Comment on the morphology of the erythrocytes.
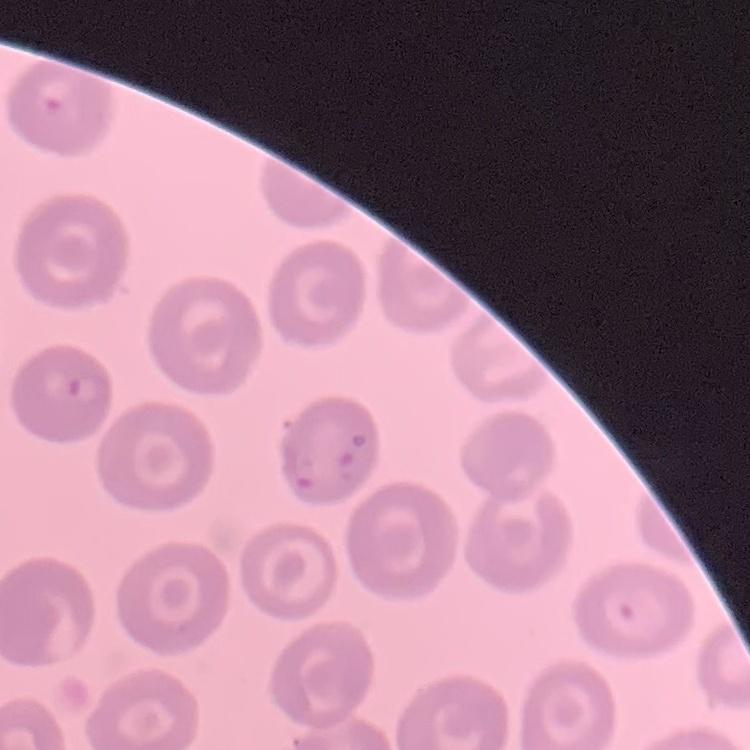

No rouleaux formation.

Stained with either Field's or Giemsa. Thin blood smear. Square crop of a larger photomicrograph.